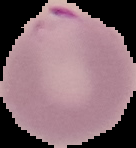

Malaria status: parasitized. The area outside the segmented cell region is set to black. From a thin blood smear. Image is 136×148 pixels.